Assess this cell for malaria.
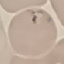
It is uninfected.

preparation = thin blood smear
image type = automatically extracted cell patch, resized to 64 × 64 pixels
stain = Giemsa
capture = smartphone camera at the microscope eyepiece